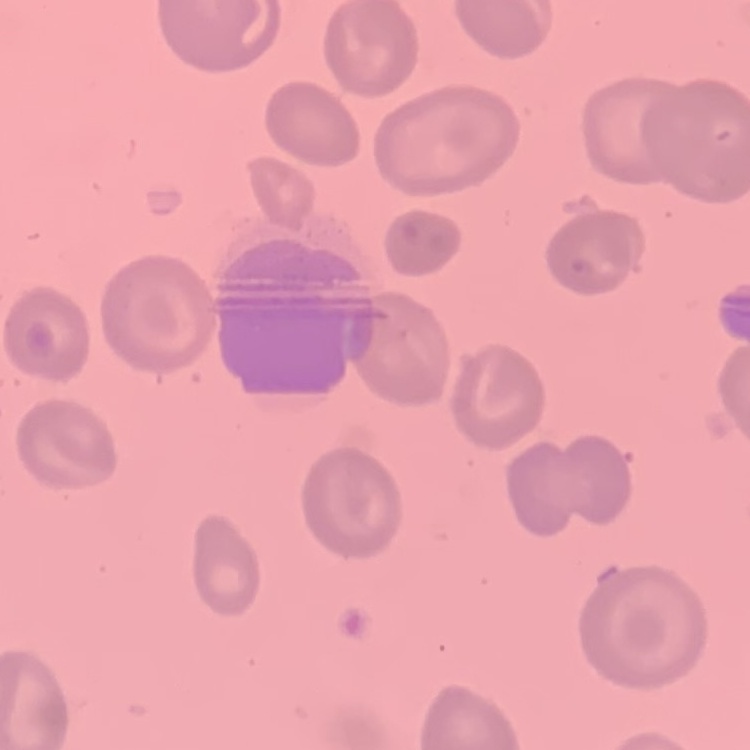 The erythrocytes exhibit no rouleaux formation. Thin peripheral smear. One tile cut from a larger photomicrograph. Field's or Giemsa stain.